Classify this cell by malaria status.
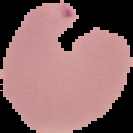
It is parasitized.

preparation = thin blood smear
image type = cell region segmented out of the field of view; surrounding area masked to black
image size = 133×133 pixels